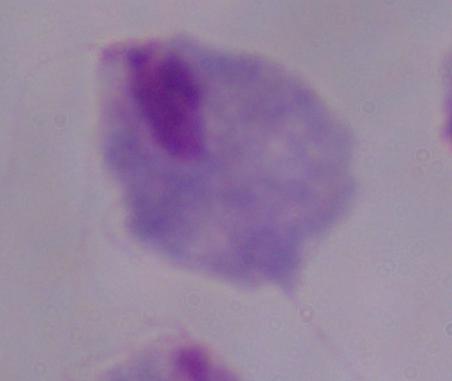

Summary:
  - Modality: photomicrograph
  - Identification: trichomonad
  - Magnification: 1000x